Outline each P. falciparum parasite and classify it by life-cycle stage.
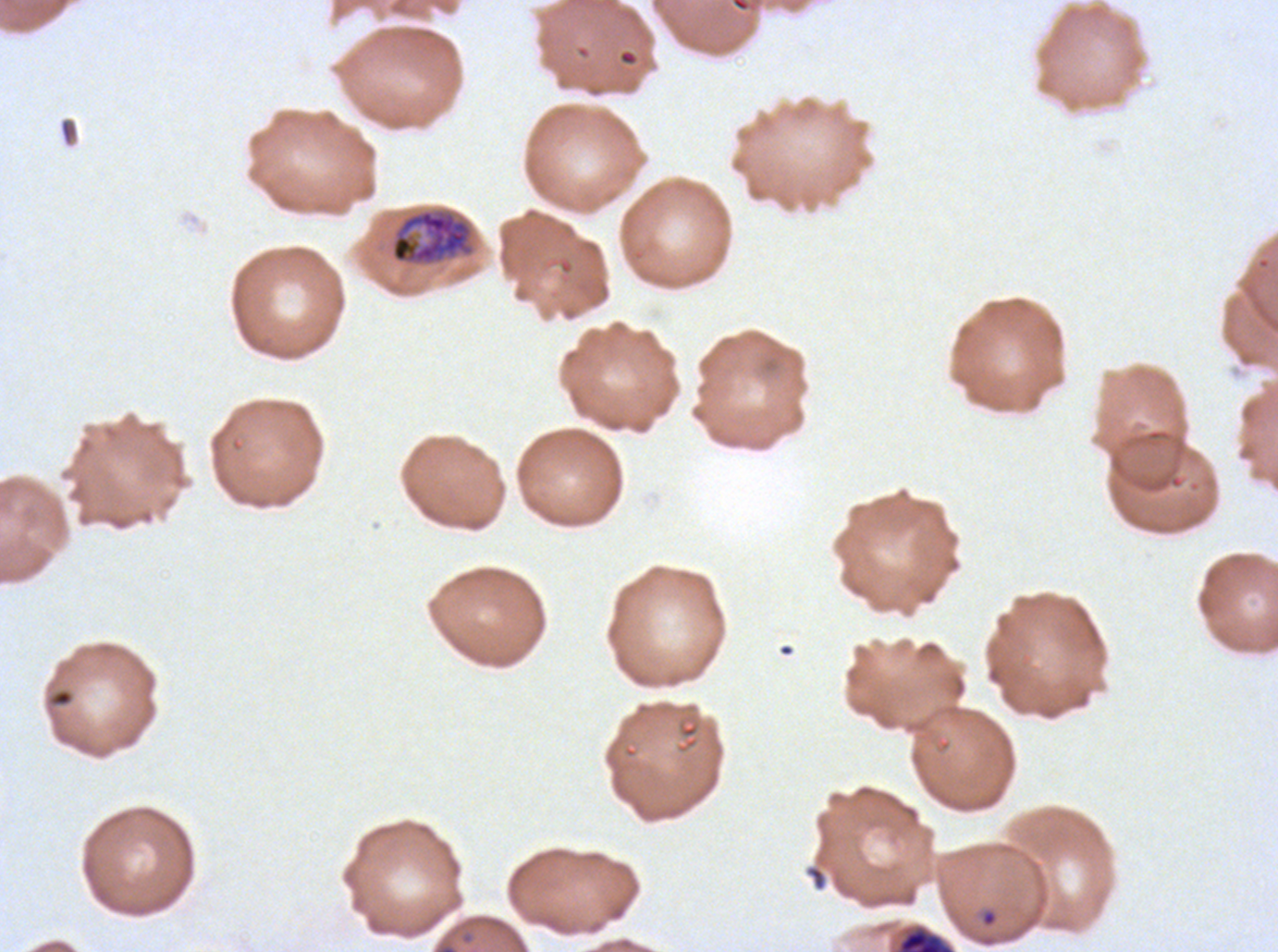

Approximate bounding rectangles given as corner coordinates in pixels from the top-left.
Rings: (x1=980, y1=909, x2=998, y2=927).
Late trophozoites: (x1=390, y1=208, x2=473, y2=265).
Late schizonts: (x1=897, y1=927, x2=954, y2=951).
No late-ring/early-trophozoite forms, mid trophozoites, early schizonts, segmenters, or gametocytes observed.

debris locations = (x1=51, y1=689, x2=73, y2=706), (x1=805, y1=865, x2=827, y2=891)
specimen = P. falciparum cultured ex vivo for 24 to 48 hours, from a patient in The Gambia
stain = Giemsa
life-cycle stages observed = ring, late trophozoite, late schizont
image size = 1278×952 pixels
preparation = thin blood smear
field of view = one sub-image of a larger composite